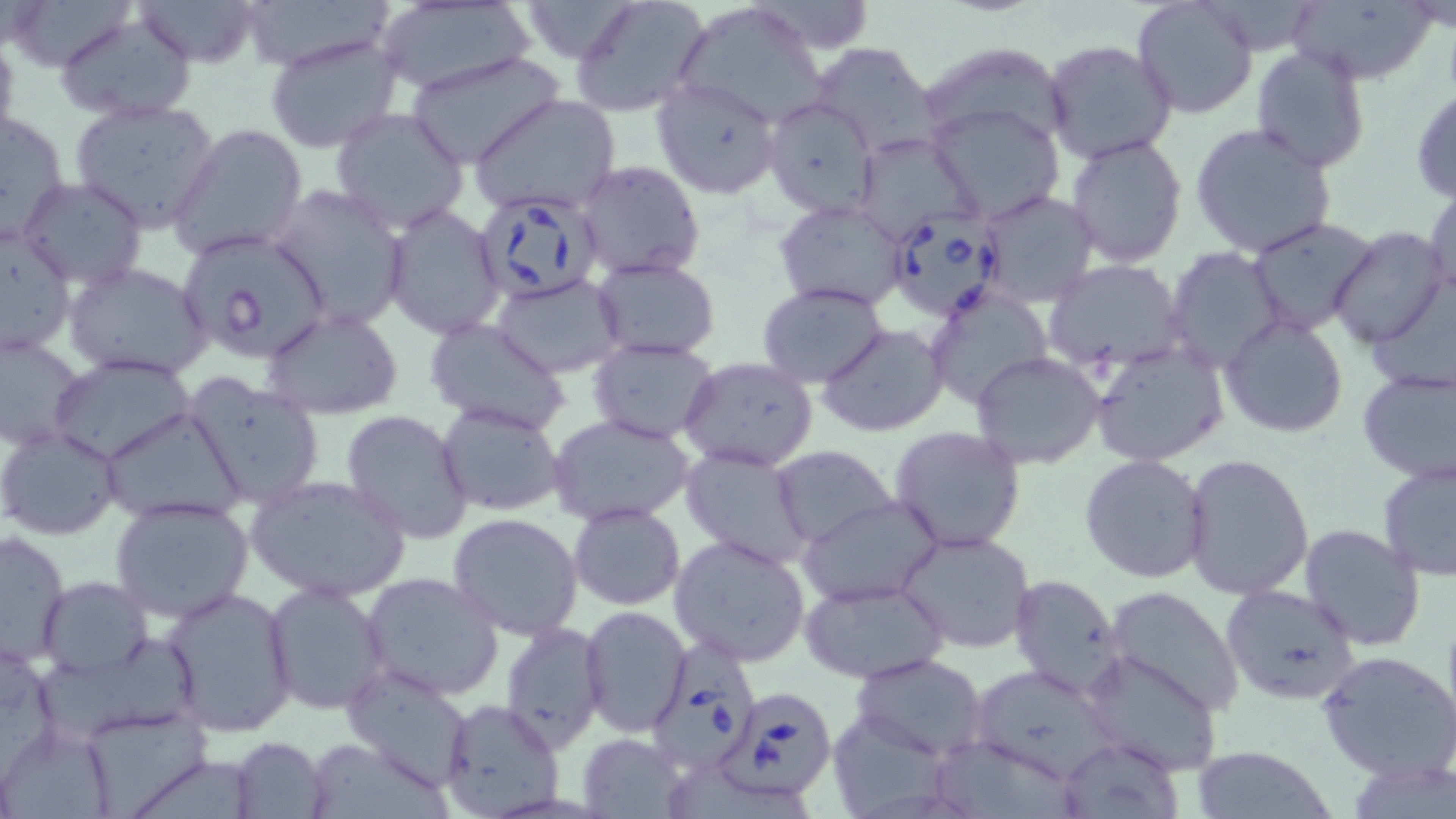 Approximate bounding boxes as [x1, y1, x2, y2] in pixels. Uninfected red blood cell locations: [3, 0, 135, 71], [136, 0, 263, 66], [237, 0, 393, 71], [571, 0, 710, 119], [1131, 0, 1259, 119], [1288, 1, 1438, 84], [378, 2, 533, 97], [670, 5, 834, 125], [54, 14, 197, 124], [1059, 18, 1253, 144], [0, 31, 21, 157], [264, 34, 403, 154], [1043, 39, 1178, 164], [807, 40, 939, 156], [925, 44, 1068, 136], [1249, 45, 1372, 174], [405, 50, 564, 168], [651, 78, 781, 199], [1410, 87, 1456, 201], [469, 95, 622, 216], [762, 97, 880, 218], [70, 98, 221, 233], [927, 103, 1066, 222], [1, 109, 71, 244], [330, 109, 470, 235], [1190, 122, 1338, 258], [170, 123, 308, 259], [855, 131, 981, 244], [1064, 134, 1187, 269], [576, 159, 706, 280], [19, 178, 148, 290], [266, 182, 410, 330], [1425, 183, 1456, 303], [976, 190, 1100, 308], [774, 199, 913, 312], [383, 205, 506, 340], [1246, 217, 1380, 336], [0, 225, 76, 356], [1329, 226, 1449, 348], [1163, 247, 1286, 370], [591, 256, 719, 361], [1044, 261, 1186, 368], [65, 262, 212, 382], [493, 274, 626, 378], [756, 283, 888, 388], [926, 285, 1054, 410], [261, 308, 404, 419], [1220, 315, 1350, 440], [425, 317, 569, 434], [817, 324, 949, 437], [0, 332, 85, 453], [587, 338, 720, 444], [1088, 340, 1231, 466], [971, 350, 1105, 469], [49, 355, 198, 466], [679, 357, 818, 472], [1357, 365, 1456, 485], [186, 376, 326, 508], [436, 402, 567, 516], [100, 407, 244, 526], [341, 410, 475, 543], [549, 413, 697, 526], [0, 425, 124, 541], [889, 425, 1026, 551], [679, 445, 818, 571], [768, 446, 897, 546], [1183, 453, 1313, 599], [1080, 454, 1209, 582], [1377, 459, 1456, 584], [246, 476, 411, 602], [110, 495, 254, 623], [799, 497, 941, 607], [568, 503, 686, 610], [447, 513, 584, 641], [1298, 522, 1426, 651], [0, 529, 70, 668], [900, 529, 1036, 655], [668, 533, 811, 668], [361, 572, 504, 700], [1007, 574, 1127, 697], [39, 577, 152, 676], [800, 578, 950, 683], [263, 582, 392, 715], [1219, 584, 1360, 704], [162, 585, 297, 738], [1103, 585, 1245, 716], [580, 606, 691, 738], [499, 620, 608, 750], [36, 640, 201, 738], [1316, 649, 1456, 781], [1080, 650, 1223, 775], [851, 653, 989, 759], [341, 662, 477, 788], [975, 667, 1118, 776], [439, 698, 566, 819], [835, 707, 946, 819], [90, 708, 206, 819], [0, 731, 122, 819], [579, 734, 686, 817], [231, 736, 330, 819], [1055, 736, 1185, 819], [941, 741, 1079, 819], [1191, 744, 1334, 818], [670, 763, 812, 819]. Babesia divergens-infected red blood cell locations: [473, 191, 605, 303], [887, 211, 1005, 321], [176, 228, 331, 361], [653, 633, 758, 772], [722, 684, 837, 801]. Slide-level diagnosis: Babesia divergens. Thin blood film. Captured at 1000x magnification. May-Grünwald-Giemsa-stained preparation. Single field of view. Light microscopy. Image is 1456×819 pixels.